Look for Plasmodium parasites.
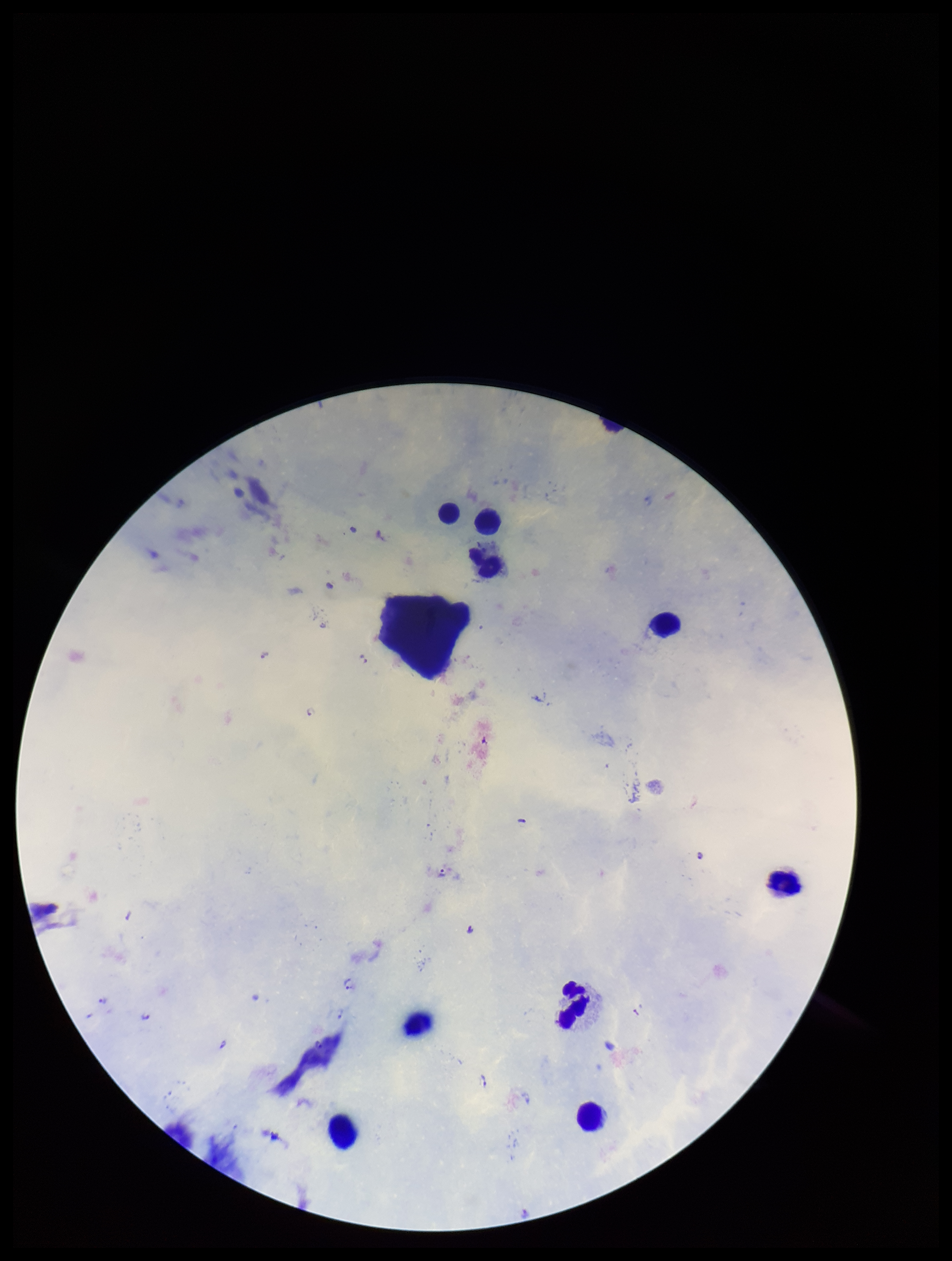

Detected.

Parasite count: 12. Patient malaria status: infected. One field from this slide. Preparation: thick smear. Smartphone photograph taken through the eyepiece of a microscope. Stained with Giemsa. Species reported for this patient: Plasmodium falciparum. Leukocyte count: 9. Image is 952×1261 pixels.